Classify this cell by malaria status.
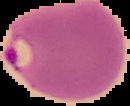

Parasitized.

image_size: 130×106 pixels
preparation: thin blood smear
image_type: segmented cell region with the area outside set to black